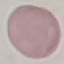

Malaria status: uninfected. Cell patch, automatically extracted from a larger field of view and resized to 64 × 64 pixels. Giemsa stain. Photographed with a smartphone camera at the microscope eyepiece. Thin smear of blood.